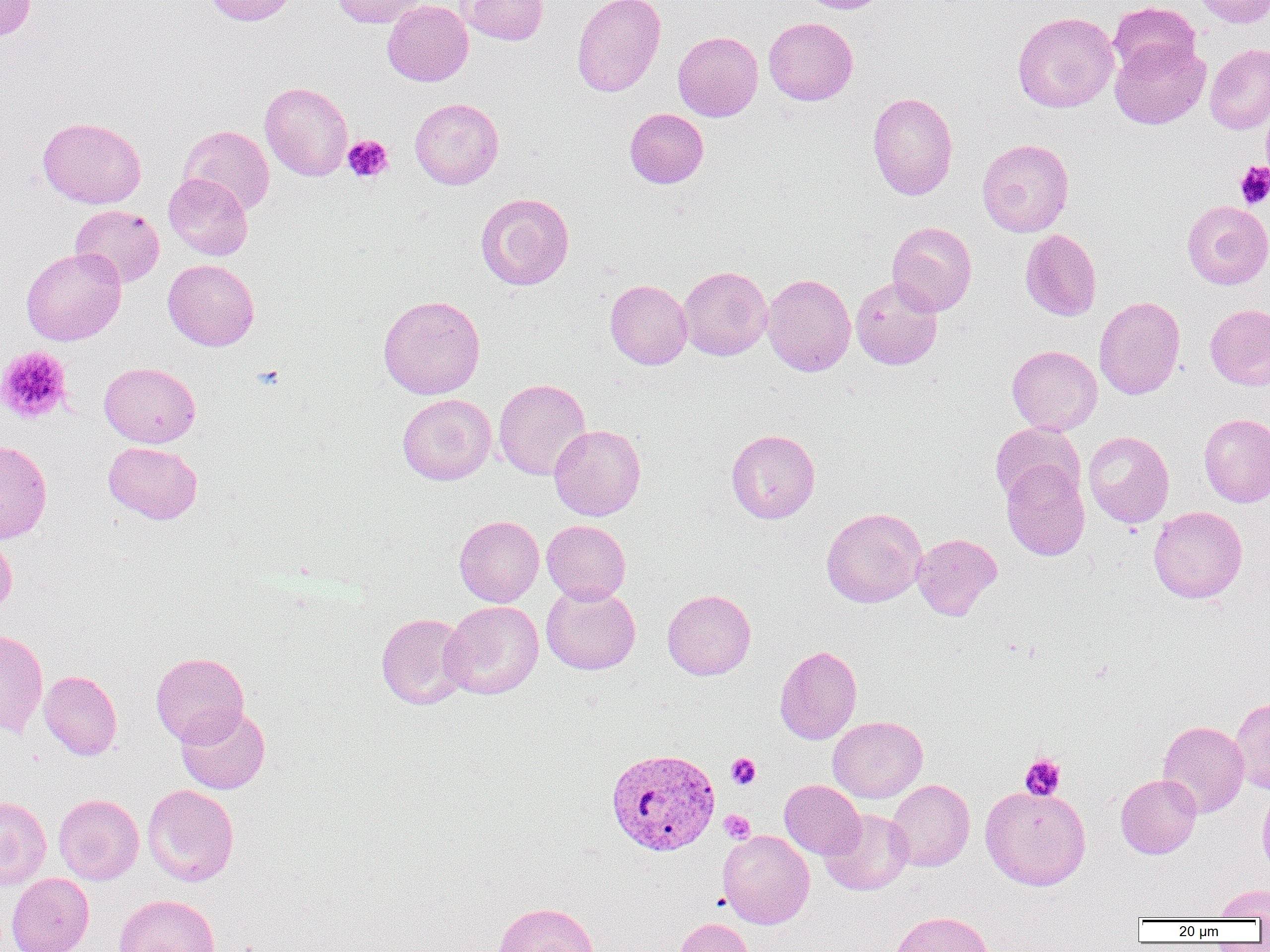 Approximate bounding boxes as (x1, y1, x2, y2) in pixels. Plasmodium vivax-infected red blood cell locations: (605, 748, 721, 856). Platelet locations: (343, 135, 393, 182), (1235, 162, 1270, 209), (0, 345, 72, 424), (726, 753, 761, 789), (1020, 754, 1065, 800), (719, 810, 755, 843). Uninfected red blood cell locations: (0, 0, 37, 40), (203, 0, 298, 26), (331, 0, 425, 27), (459, 0, 549, 45), (571, 0, 666, 97), (798, 0, 892, 14), (1192, 0, 1270, 28), (382, 1, 473, 86), (1108, 2, 1201, 80), (1013, 11, 1119, 113), (763, 17, 858, 105), (673, 31, 763, 121), (1110, 38, 1210, 130), (1204, 43, 1270, 134), (260, 81, 353, 181), (867, 92, 958, 200), (410, 98, 503, 189), (625, 108, 709, 188), (37, 117, 146, 208), (179, 125, 274, 214), (977, 138, 1074, 237), (163, 173, 253, 260), (475, 192, 574, 290), (1182, 200, 1270, 289), (70, 205, 165, 288), (887, 221, 977, 316), (1020, 229, 1102, 321), (21, 247, 126, 346), (163, 259, 260, 351), (678, 266, 772, 361), (762, 273, 856, 376), (850, 276, 943, 370), (605, 279, 692, 369), (378, 295, 485, 400), (1094, 296, 1186, 400), (1205, 304, 1270, 390), (1007, 345, 1102, 435), (99, 362, 200, 447), (494, 378, 591, 481), (397, 394, 496, 485), (1199, 414, 1270, 506), (990, 422, 1085, 508), (549, 424, 646, 520), (726, 429, 820, 523), (1083, 431, 1174, 527), (0, 440, 52, 543), (103, 441, 202, 524), (1001, 463, 1090, 560), (1149, 506, 1247, 603), (821, 507, 927, 608), (454, 515, 544, 607), (542, 520, 631, 604), (912, 533, 1002, 620), (0, 534, 17, 617), (541, 584, 641, 675), (662, 589, 756, 680), (440, 601, 543, 700), (376, 612, 472, 710), (0, 627, 48, 737), (774, 645, 862, 744), (151, 652, 249, 746), (39, 670, 122, 760), (1229, 697, 1270, 794), (176, 705, 270, 794), (828, 716, 927, 803), (1157, 720, 1249, 817), (1116, 774, 1202, 858), (886, 779, 974, 872), (780, 780, 865, 859), (142, 784, 239, 886), (980, 785, 1091, 890), (1257, 787, 1270, 879), (53, 794, 144, 885), (0, 796, 51, 890), (820, 809, 914, 895), (717, 830, 815, 929), (6, 873, 94, 952), (1214, 884, 1270, 919), (113, 894, 220, 952), (492, 901, 600, 952), (890, 910, 994, 952), (673, 917, 754, 952). Slide-level diagnosis: Plasmodium vivax. Single field of view. Thin blood smear. Light microscopy. 1000x magnification. Image is 1270×952 pixels.